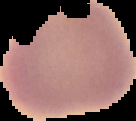
Summary:
  - Image size: 136×121 pixels
  - Image type: segmented cell region on a black background
  - Malaria status: uninfected
  - Preparation: thin blood smear